Locate every blood parasite and identify its species.
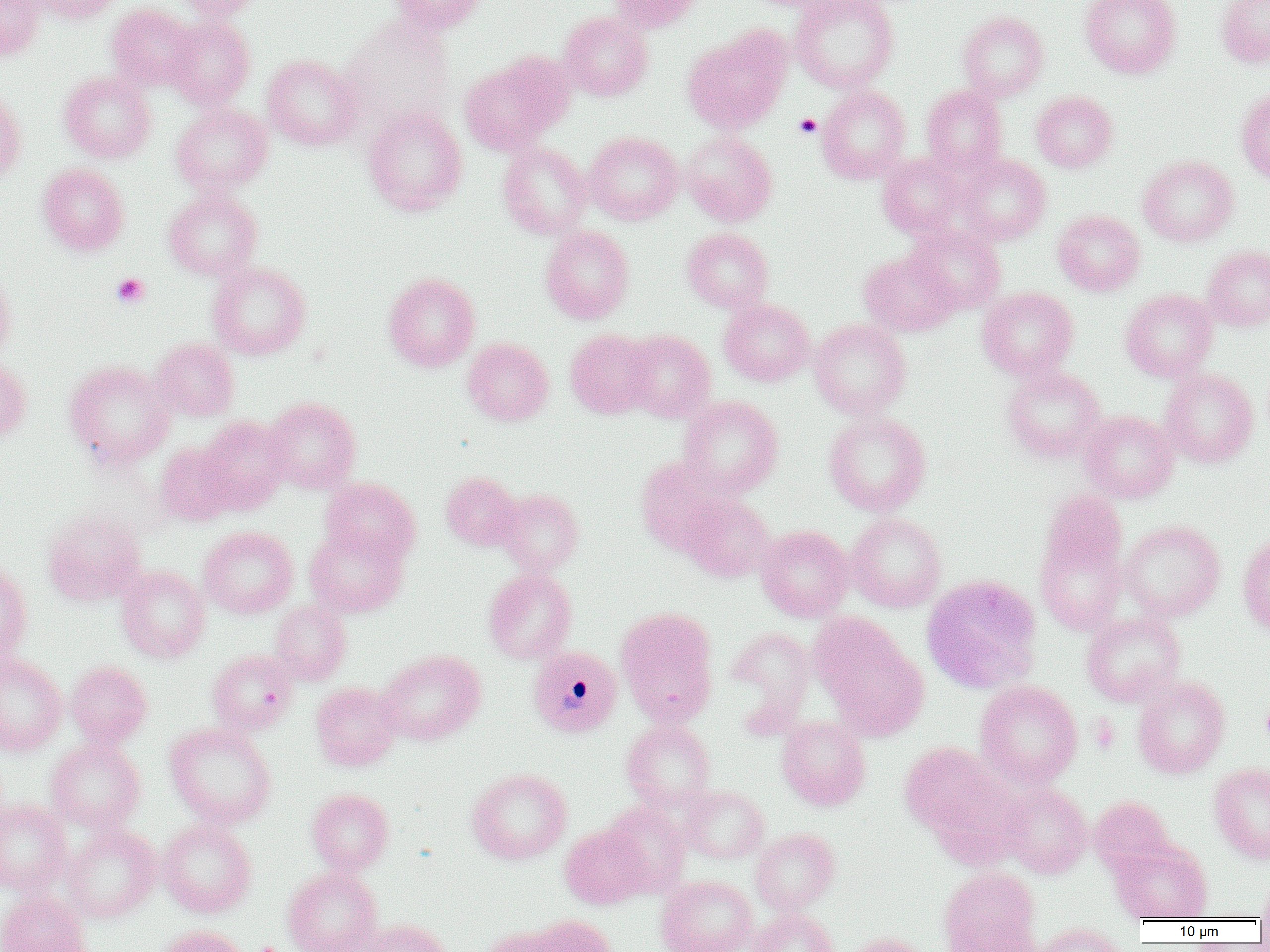

Approximate bounding boxes as named x1/y1/x2/y2 corners in pixels.
Plasmodium malariae-infected red blood cells: (x1=527, y1=645, x2=623, y2=737).
No Plasmodium falciparum, Plasmodium ovale, Plasmodium vivax, Babesia divergens, or Trypanosoma brucei observed.

Summary:
  - Uninfected red blood cell locations: (x1=0, y1=0, x2=45, y2=60), (x1=27, y1=0, x2=122, y2=24), (x1=173, y1=0, x2=265, y2=20), (x1=387, y1=0, x2=487, y2=35), (x1=609, y1=0, x2=707, y2=32), (x1=790, y1=0, x2=899, y2=93), (x1=1081, y1=0, x2=1181, y2=79), (x1=1216, y1=0, x2=1270, y2=67), (x1=107, y1=3, x2=197, y2=91), (x1=558, y1=11, x2=653, y2=101), (x1=958, y1=11, x2=1049, y2=100), (x1=166, y1=17, x2=255, y2=110), (x1=340, y1=17, x2=456, y2=131), (x1=683, y1=27, x2=790, y2=134), (x1=459, y1=54, x2=569, y2=154), (x1=262, y1=55, x2=362, y2=150), (x1=60, y1=71, x2=155, y2=162), (x1=817, y1=85, x2=911, y2=183), (x1=921, y1=85, x2=1007, y2=173), (x1=1236, y1=86, x2=1270, y2=186), (x1=0, y1=87, x2=26, y2=184), (x1=1032, y1=91, x2=1117, y2=172), (x1=171, y1=104, x2=273, y2=195), (x1=363, y1=107, x2=467, y2=216), (x1=680, y1=130, x2=778, y2=226), (x1=584, y1=132, x2=683, y2=224), (x1=498, y1=141, x2=591, y2=239), (x1=877, y1=152, x2=968, y2=238), (x1=959, y1=154, x2=1051, y2=244), (x1=1138, y1=154, x2=1238, y2=246), (x1=37, y1=163, x2=129, y2=255), (x1=164, y1=190, x2=262, y2=280), (x1=1053, y1=210, x2=1145, y2=296), (x1=907, y1=224, x2=1005, y2=314), (x1=540, y1=225, x2=634, y2=324), (x1=682, y1=228, x2=774, y2=313), (x1=1202, y1=245, x2=1270, y2=331), (x1=859, y1=250, x2=960, y2=336), (x1=208, y1=261, x2=311, y2=359), (x1=0, y1=268, x2=17, y2=361), (x1=383, y1=272, x2=480, y2=372), (x1=977, y1=286, x2=1078, y2=380), (x1=1120, y1=289, x2=1218, y2=381), (x1=719, y1=299, x2=814, y2=385), (x1=809, y1=319, x2=911, y2=419), (x1=565, y1=329, x2=656, y2=418), (x1=621, y1=330, x2=716, y2=423), (x1=151, y1=338, x2=239, y2=421), (x1=463, y1=338, x2=553, y2=426), (x1=0, y1=356, x2=31, y2=444), (x1=64, y1=360, x2=173, y2=469), (x1=1002, y1=364, x2=1106, y2=463), (x1=1160, y1=368, x2=1259, y2=467), (x1=678, y1=395, x2=783, y2=496), (x1=264, y1=397, x2=361, y2=493), (x1=1080, y1=410, x2=1178, y2=504), (x1=823, y1=412, x2=931, y2=515), (x1=199, y1=416, x2=293, y2=511), (x1=154, y1=442, x2=238, y2=526), (x1=636, y1=455, x2=735, y2=553), (x1=441, y1=472, x2=522, y2=551), (x1=320, y1=477, x2=421, y2=565), (x1=495, y1=489, x2=584, y2=574), (x1=1039, y1=489, x2=1127, y2=583), (x1=681, y1=495, x2=776, y2=582), (x1=42, y1=509, x2=146, y2=605), (x1=847, y1=512, x2=946, y2=612), (x1=1034, y1=518, x2=1128, y2=637), (x1=1119, y1=520, x2=1226, y2=621), (x1=756, y1=524, x2=854, y2=621), (x1=199, y1=526, x2=297, y2=618), (x1=305, y1=527, x2=407, y2=618), (x1=1238, y1=531, x2=1270, y2=636), (x1=0, y1=560, x2=32, y2=664), (x1=116, y1=565, x2=210, y2=663), (x1=483, y1=568, x2=577, y2=664), (x1=922, y1=575, x2=1043, y2=693), (x1=270, y1=600, x2=352, y2=685), (x1=615, y1=607, x2=719, y2=725), (x1=1081, y1=612, x2=1186, y2=706), (x1=814, y1=619, x2=929, y2=740), (x1=725, y1=626, x2=815, y2=725), (x1=208, y1=649, x2=299, y2=734), (x1=377, y1=650, x2=485, y2=745), (x1=0, y1=655, x2=68, y2=756), (x1=66, y1=661, x2=152, y2=747), (x1=1132, y1=675, x2=1230, y2=779), (x1=974, y1=680, x2=1082, y2=788), (x1=311, y1=682, x2=402, y2=770), (x1=777, y1=717, x2=871, y2=811), (x1=621, y1=719, x2=716, y2=809), (x1=165, y1=723, x2=276, y2=827), (x1=46, y1=737, x2=146, y2=832), (x1=899, y1=741, x2=1005, y2=837), (x1=1209, y1=762, x2=1270, y2=864), (x1=467, y1=767, x2=572, y2=864), (x1=999, y1=784, x2=1093, y2=878), (x1=681, y1=786, x2=769, y2=863), (x1=306, y1=788, x2=394, y2=873), (x1=1089, y1=796, x2=1174, y2=874), (x1=0, y1=799, x2=72, y2=894), (x1=601, y1=801, x2=691, y2=896), (x1=156, y1=818, x2=257, y2=918), (x1=62, y1=824, x2=160, y2=922), (x1=559, y1=825, x2=650, y2=909), (x1=750, y1=828, x2=840, y2=914), (x1=1111, y1=840, x2=1213, y2=922), (x1=938, y1=865, x2=1040, y2=952), (x1=283, y1=866, x2=382, y2=952), (x1=1258, y1=873, x2=1270, y2=924), (x1=656, y1=875, x2=756, y2=952), (x1=0, y1=890, x2=92, y2=952), (x1=750, y1=908, x2=841, y2=952), (x1=515, y1=914, x2=618, y2=952), (x1=941, y1=917, x2=1042, y2=952), (x1=359, y1=919, x2=452, y2=952), (x1=1033, y1=922, x2=1127, y2=952), (x1=157, y1=925, x2=251, y2=952), (x1=842, y1=932, x2=934, y2=952)
  - Platelet locations: (x1=795, y1=114, x2=821, y2=138), (x1=111, y1=273, x2=150, y2=309), (x1=1261, y1=700, x2=1270, y2=745), (x1=250, y1=942, x2=287, y2=952)
  - Slide-level diagnosis: Plasmodium malariae
  - Field of view: one of a larger specimen
  - Preparation: thin blood film
  - Image size: 1270×952 pixels
  - Modality: light microscopy
  - Magnification: 1000x